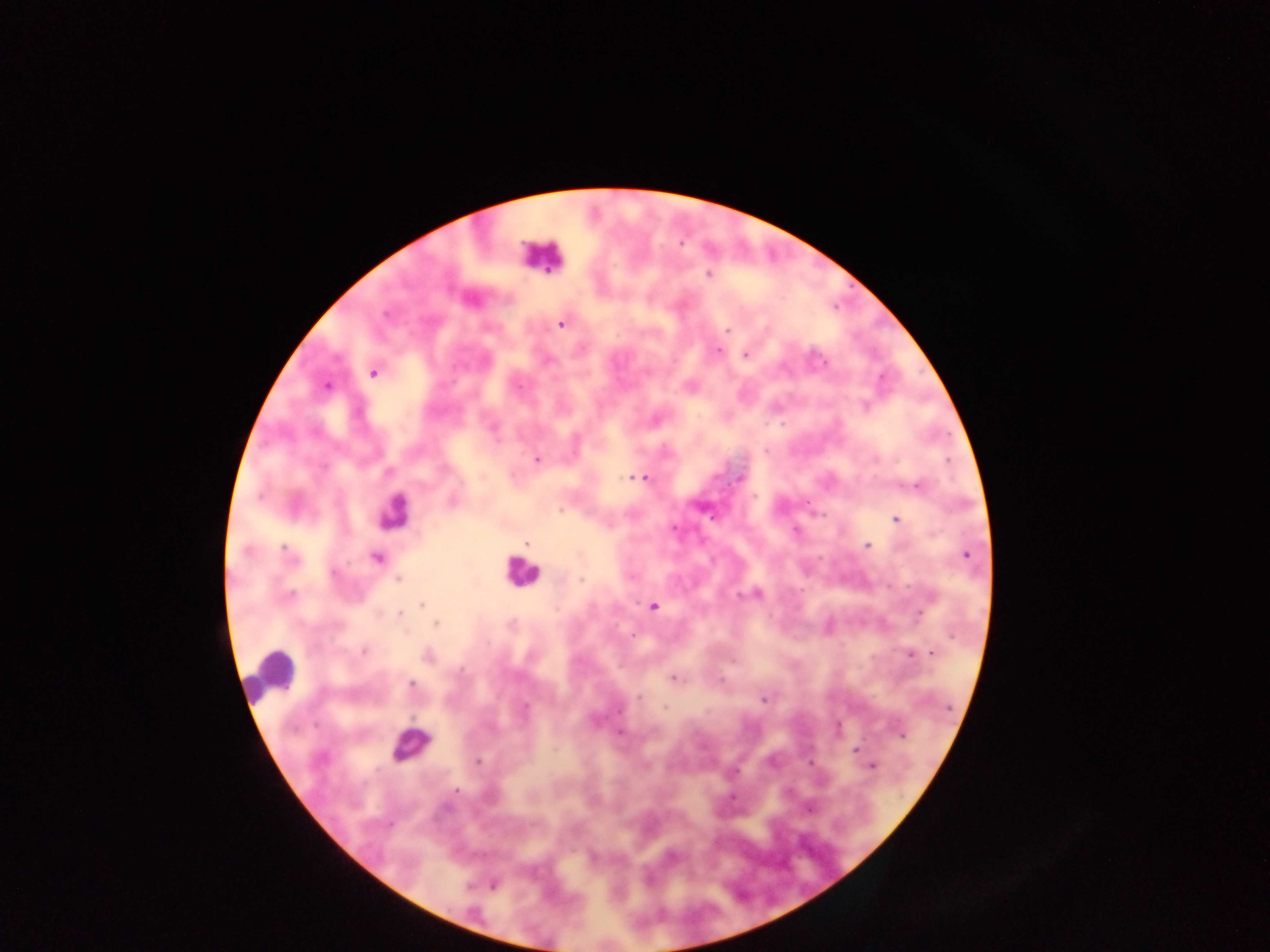

Approximate centers as [x, y] in pixels.
Summary:
  - Leukocyte locations: [541, 256], [392, 509], [521, 571], [266, 668], [409, 744]
  - Plasmodium parasite locations: [709, 275], [561, 324], [727, 330], [717, 351], [746, 355], [373, 373], [326, 385], [518, 387], [865, 407], [494, 428], [765, 452], [537, 459], [876, 460], [627, 477], [645, 477], [741, 479], [918, 485], [561, 509], [896, 519], [526, 544], [868, 545], [247, 551], [285, 551], [966, 555], [377, 558], [334, 573], [581, 579], [398, 580], [757, 593], [740, 595], [288, 596], [422, 604], [653, 606], [920, 613], [400, 614], [435, 624], [634, 636], [364, 651], [932, 653], [909, 654], [428, 655], [674, 679], [721, 681], [412, 684], [639, 697], [763, 700], [665, 708], [619, 711], [620, 732], [903, 735], [856, 749], [477, 762], [872, 765], [456, 790], [810, 809], [671, 856], [494, 885]
  - Capture: mobile-phone photograph through a microscope
  - Image size: 1270×952 pixels
  - Country: Ghana
  - Field of view: single
  - Preparation: thick blood film